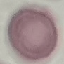
Summary:
  - Malaria status: uninfected
  - Preparation: thin blood film
  - Stain: Giemsa
  - Image type: automatically extracted cell patch, resized to 64 × 64 pixels
  - Capture: smartphone camera at the microscope eyepiece